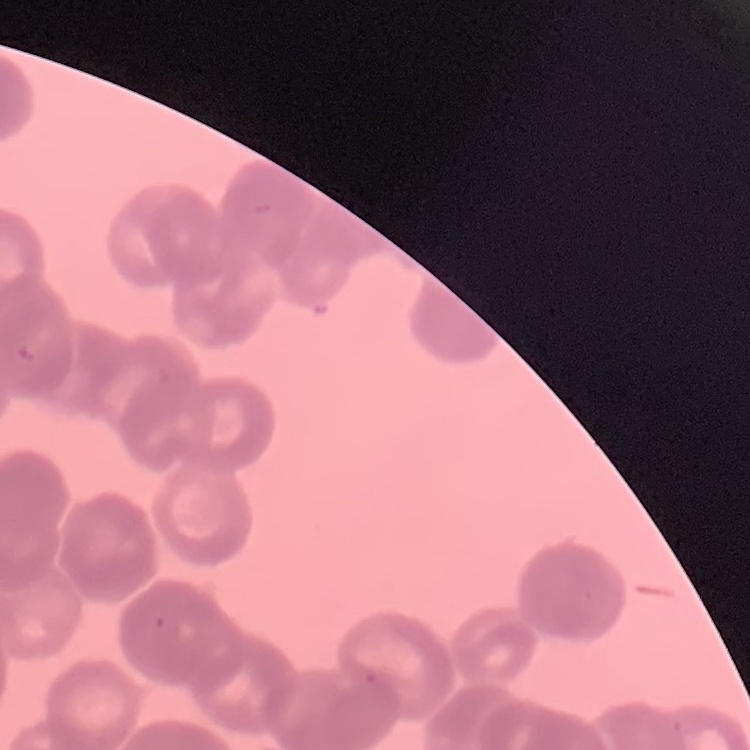

The erythrocytes exhibit rouleaux formation. One tile cut from a larger photomicrograph. Stained with either Field's or Giemsa. Thin blood smear.